Identify the parasite.
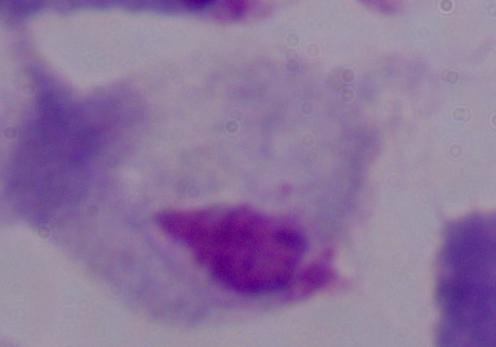

This is a trichomonad.

magnification = 1000x
modality = micrograph